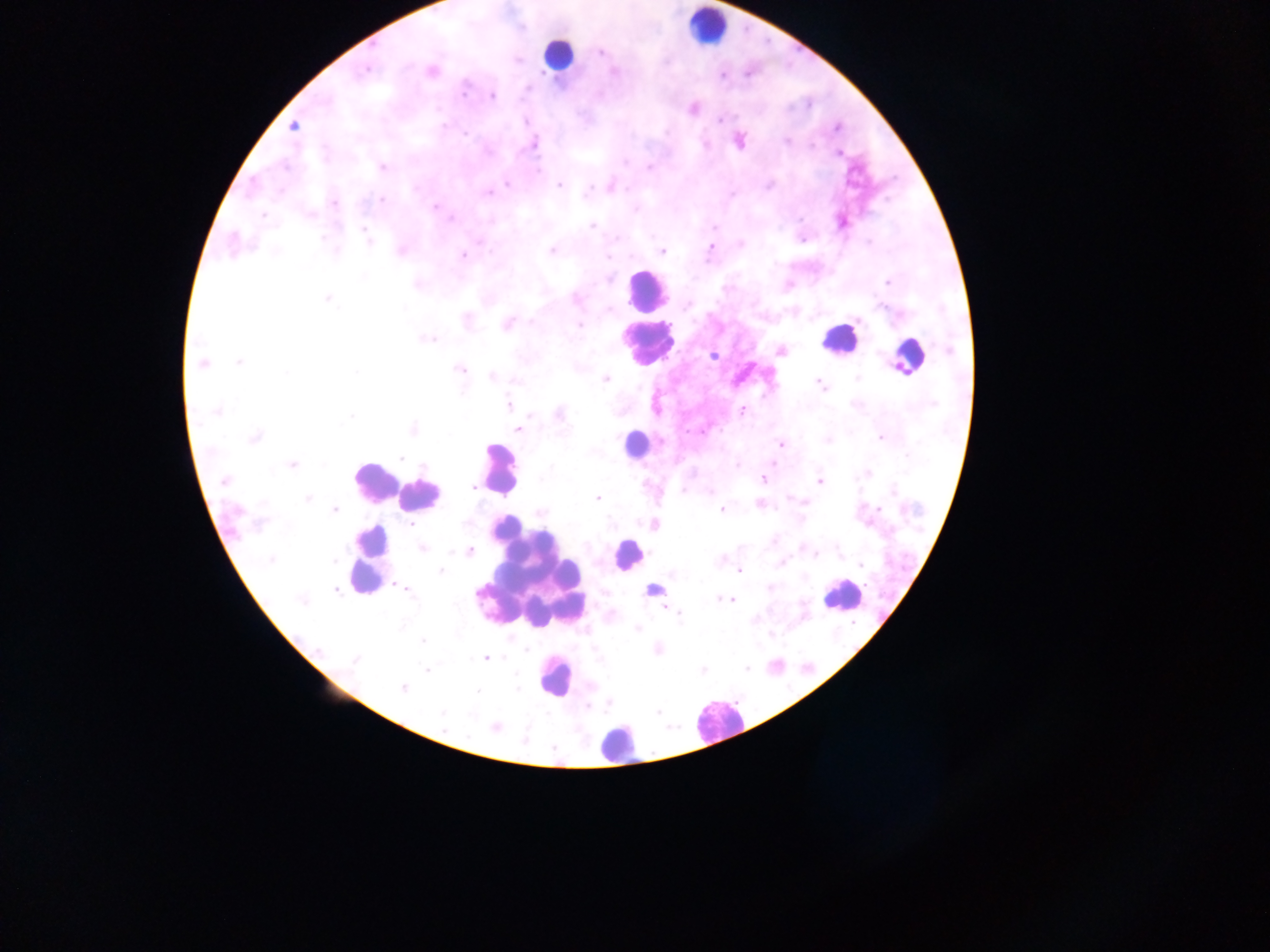

Approximate centers as x y in pixels. Malaria parasite locations: 601 52; 365 70; 431 70; 615 72; 723 76; 464 92; 491 96; 693 109; 525 121; 719 121; 442 126; 293 127; 837 127; 739 141; 787 141; 705 144; 534 145; 488 151; 839 153; 624 162; 382 167; 649 168; 537 172; 507 184; 559 185; 769 185; 611 187; 588 191; 488 192; 381 199; 334 203; 435 207; 636 209; 310 214; 263 215; 451 219; 799 219; 842 223; 593 225; 366 234; 323 237; 803 240; 232 244; 711 247; 552 251; 401 252; 662 252; 463 255; 608 279; 887 282; 417 285; 328 299; 576 299; 688 305; 467 321; 508 324; 579 325; 429 340; 781 351; 713 356; 240 362; 202 363; 460 369; 356 372; 493 376; 605 379; 515 381; 819 383; 509 405; 216 411; 741 411; 560 415; 351 416; 413 429; 519 429; 255 437; 881 437; 780 444; 402 457; 291 465; 736 465; 550 467; 763 479; 224 480; 819 481; 473 487; 892 490; 710 492; 597 498; 307 499; 804 503; 760 505; 879 508; 335 510; 721 510; 539 511; 260 523; 410 525; 653 525; 422 548; 469 552; 815 554; 719 559; 271 560; 335 561; 781 564; 860 565; 440 571; 740 571; 653 587; 770 588; 406 589; 335 590; 719 599; 732 600; 301 601; 678 615; 638 628; 423 641; 319 650; 527 650; 486 658; 354 660; 746 668; 703 669; 427 670; 402 688; 518 688; 477 691; 658 712; 442 713; 495 728. Leukocyte locations: 706 27; 557 54; 645 289; 838 339; 646 344; 907 355; 637 443; 498 469; 375 481; 420 493; 627 554; 370 560; 528 574; 842 594; 554 677; 717 721; 615 744. Collected in Ghana. One field of view. Thick blood film. Image is 1270×952 pixels. Mobile-phone photograph taken through the microscope.